Name the cell type shown.
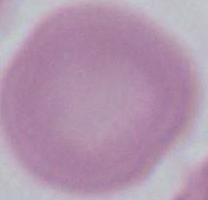

An erythrocyte.

Summary:
  - Magnification: 1000x
  - Modality: micrograph